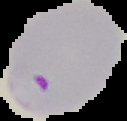
Image is 127×121 pixels. From a thin blood film. The area outside the segmented cell region is set to black. Result: Plasmodium parasites detected.